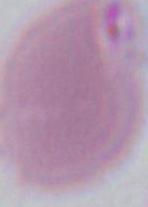 Photomicrograph. 1000x magnification. A red blood cell is shown.